Report the malaria status of this cell.
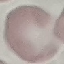

It is uninfected.

Summary:
  - Image type: automatically extracted cell patch, resized to 64 × 64 pixels
  - Preparation: thin blood film
  - Stain: Giemsa
  - Capture: smartphone camera at the microscope eyepiece